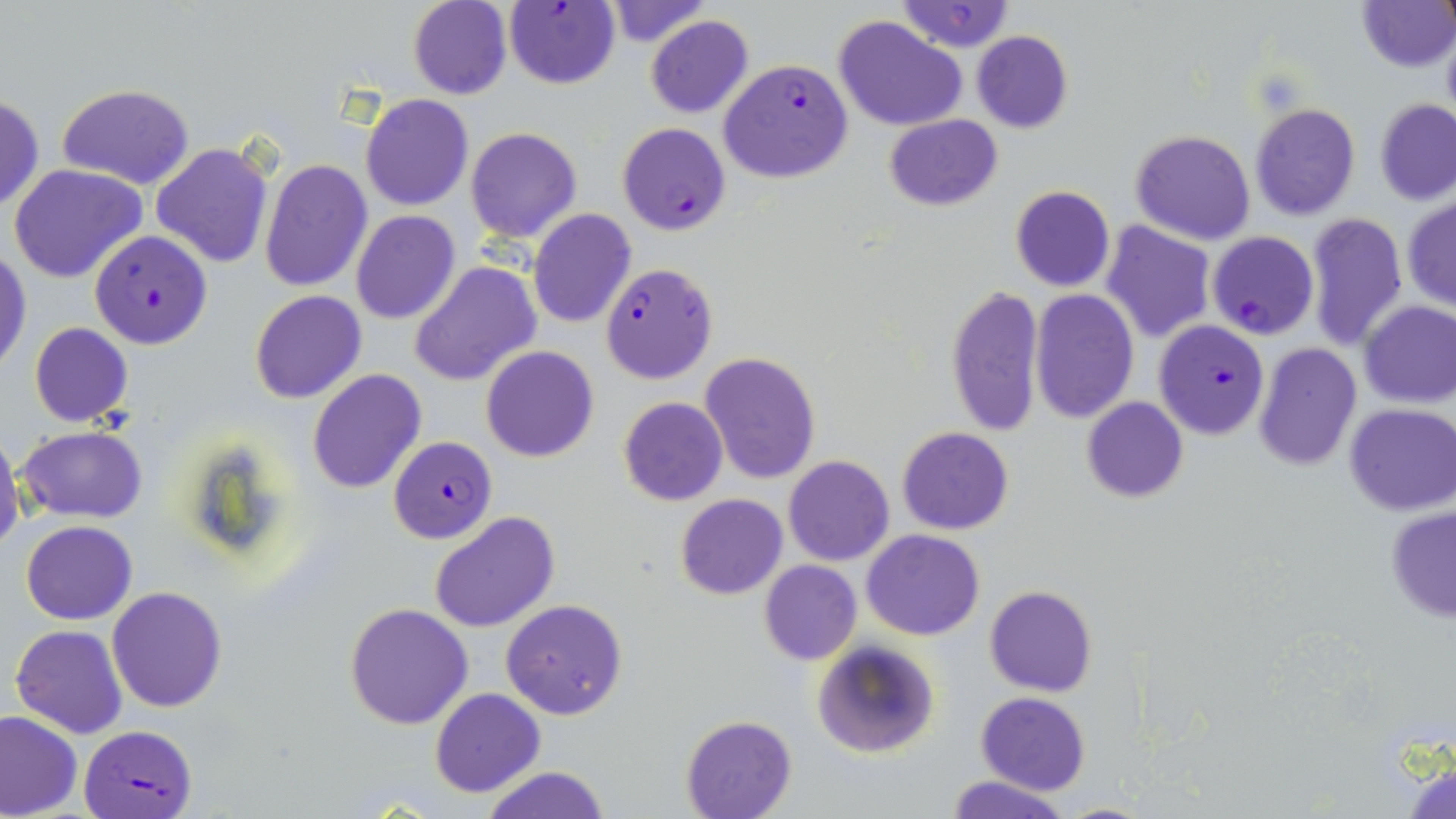
Summary:
  - Coordinate format: approximate bounding boxes as (x1,y1)-(x2,y2) corner pairs in pixels
  - Uninfected red blood cell locations: (897,0)-(1017,53), (1357,0)-(1455,72), (407,1)-(512,99), (603,1)-(709,48), (645,15)-(753,119), (834,16)-(967,131), (972,30)-(1073,132), (58,83)-(194,189), (1,92)-(45,214), (360,95)-(474,211), (1375,99)-(1456,205), (1250,103)-(1360,220), (883,113)-(1001,211), (465,127)-(582,243), (1130,129)-(1256,244), (152,140)-(274,268), (259,160)-(372,291), (8,162)-(147,284), (1010,185)-(1115,291), (1402,195)-(1456,312), (528,208)-(637,327), (351,211)-(460,325), (1303,212)-(1409,352), (1101,222)-(1215,343), (0,246)-(32,377), (410,261)-(541,388), (945,285)-(1044,438), (250,290)-(367,404), (1031,290)-(1138,423), (1360,300)-(1456,408), (30,322)-(132,427), (1253,342)-(1362,471), (481,346)-(598,463), (699,351)-(820,486), (308,369)-(426,494), (617,396)-(729,506), (1082,397)-(1187,503), (1343,404)-(1455,516), (17,425)-(147,522), (897,426)-(1014,534), (0,431)-(25,559), (784,456)-(894,567), (675,494)-(787,600), (1386,504)-(1456,623), (429,511)-(560,633), (20,520)-(137,625), (863,529)-(984,640), (760,560)-(862,665), (984,585)-(1098,697), (107,587)-(229,713), (501,598)-(628,721), (344,603)-(474,730), (10,625)-(128,739), (811,639)-(939,759), (430,687)-(545,797), (975,691)-(1090,795), (0,711)-(81,818), (681,714)-(796,818), (1403,757)-(1456,818), (481,766)-(610,819), (945,775)-(1069,819), (1049,802)-(1163,818)
  - Plasmodium falciparum-infected red blood cell locations: (503,2)-(622,90), (718,59)-(853,183), (618,122)-(732,236), (89,229)-(213,349), (1208,231)-(1319,340), (599,262)-(719,384), (1153,320)-(1270,439), (387,435)-(496,544), (79,726)-(196,818)
  - Slide-level diagnosis: Plasmodium falciparum
  - Magnification: 1000x
  - Stain: May-Grünwald-Giemsa
  - Field of view: single
  - Preparation: thin blood smear
  - Image size: 1456×819 pixels
  - Modality: optical microscopy